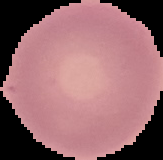
Summary:
  - Result: negative for malaria parasites
  - Image size: 163×160 pixels
  - Image type: segmented cell region with the area outside set to black
  - Preparation: thin blood film